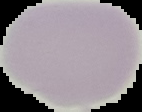

Result: no malaria parasites detected. Image is 142×112 pixels. The area outside the segmented cell region is set to black. From a thin blood film.